Report the malaria status of this cell.
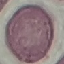

It is uninfected.

Giemsa stain. Thin blood smear. Automatically extracted cell patch, resized to 64 × 64 pixels. Acquired by smartphone through the microscope eyepiece.